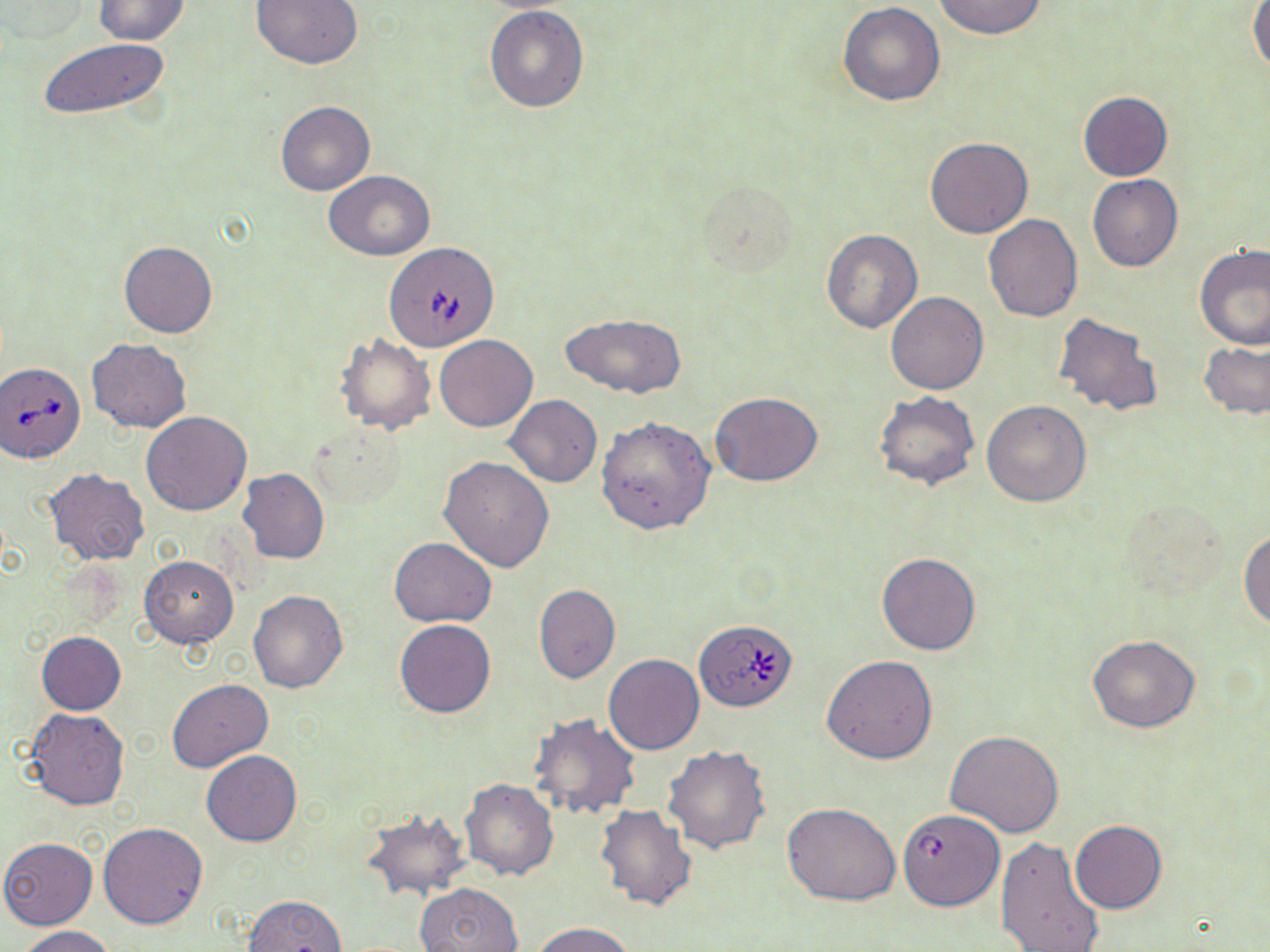

{
  "slide_level_diagnosis": "Babesia divergens",
  "field_of_view": "one of a larger specimen",
  "image_size": "1270×952 pixels",
  "magnification": "1000x",
  "uninfected_red_blood_cell_locations": "approximate bounding boxes as [x1, y1, x2, y2] in pixels: [1, 0, 90, 43], [91, 0, 191, 45], [250, 0, 363, 70], [933, 0, 1047, 42], [837, 2, 946, 105], [1248, 3, 1270, 73], [483, 5, 589, 113], [37, 36, 171, 121], [1078, 92, 1172, 181], [276, 101, 375, 194], [925, 136, 1032, 238], [323, 171, 434, 260], [1087, 174, 1183, 273], [696, 178, 803, 280], [983, 214, 1083, 322], [820, 230, 924, 333], [120, 241, 217, 338], [1193, 243, 1270, 350], [885, 292, 989, 395], [1052, 311, 1164, 419], [561, 312, 686, 399], [335, 334, 437, 435], [435, 335, 537, 432], [86, 338, 191, 433], [1199, 342, 1270, 420], [710, 391, 823, 487], [874, 391, 980, 490], [504, 395, 603, 487], [981, 399, 1092, 506], [141, 412, 251, 516], [596, 416, 716, 534], [312, 425, 408, 509], [439, 456, 555, 572], [237, 468, 329, 565], [46, 469, 149, 565], [1239, 530, 1269, 629], [389, 538, 497, 627], [876, 552, 981, 656], [138, 556, 238, 647], [534, 584, 621, 683], [248, 590, 348, 693], [394, 619, 495, 717], [36, 631, 126, 714], [1087, 635, 1199, 733], [604, 654, 704, 754], [822, 654, 939, 765], [166, 679, 272, 773], [22, 708, 130, 810], [527, 715, 639, 823], [946, 731, 1065, 837], [662, 744, 773, 854], [201, 749, 302, 847], [461, 778, 558, 879], [781, 802, 901, 906], [594, 803, 698, 912], [362, 811, 470, 901], [1069, 818, 1166, 914], [99, 823, 208, 929], [996, 835, 1104, 952], [0, 837, 98, 929], [417, 882, 523, 952], [241, 894, 347, 951], [534, 922, 632, 952], [18, 926, 118, 952]",
  "babesia_divergens_infected_red_blood_cell_locations": "approximate bounding boxes as [x1, y1, x2, y2] in pixels: [382, 243, 501, 355], [1, 361, 85, 464], [695, 619, 798, 711], [898, 810, 1007, 916]",
  "preparation": "thin blood smear",
  "stain": "May-Grünwald-Giemsa",
  "modality": "light microscopy"
}